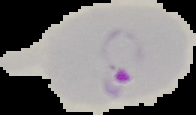 Image is 196×115 pixels. Segmented cell region on a black background. From a thin blood film. Result: malaria parasites identified.